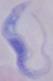
A trypanosome is seen. Micrograph. Captured at 1000x magnification.